Comment on the morphology of the erythrocytes.
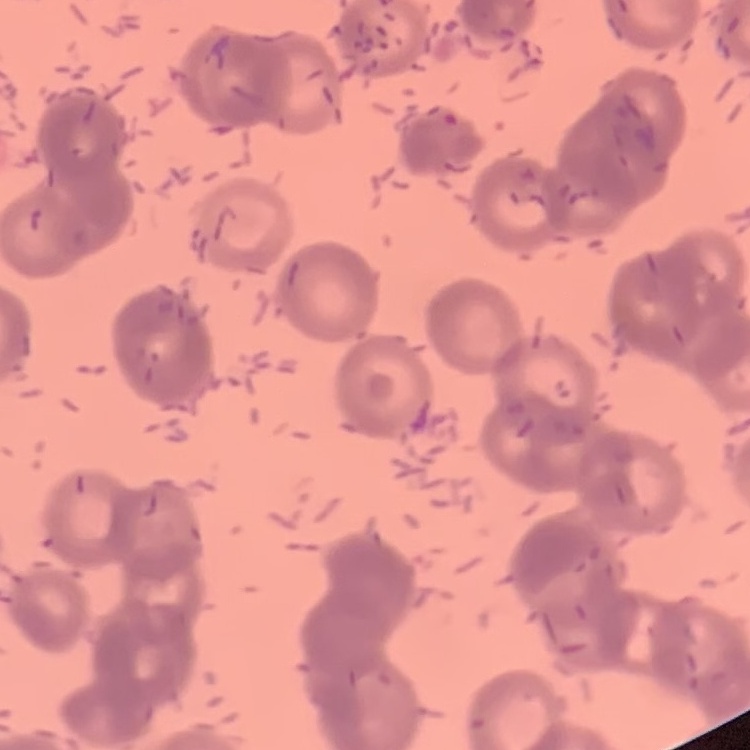

They show rouleaux formation.

image_type: square crop of a larger photomicrograph
preparation: thin blood smear
stain: Field's or Giemsa